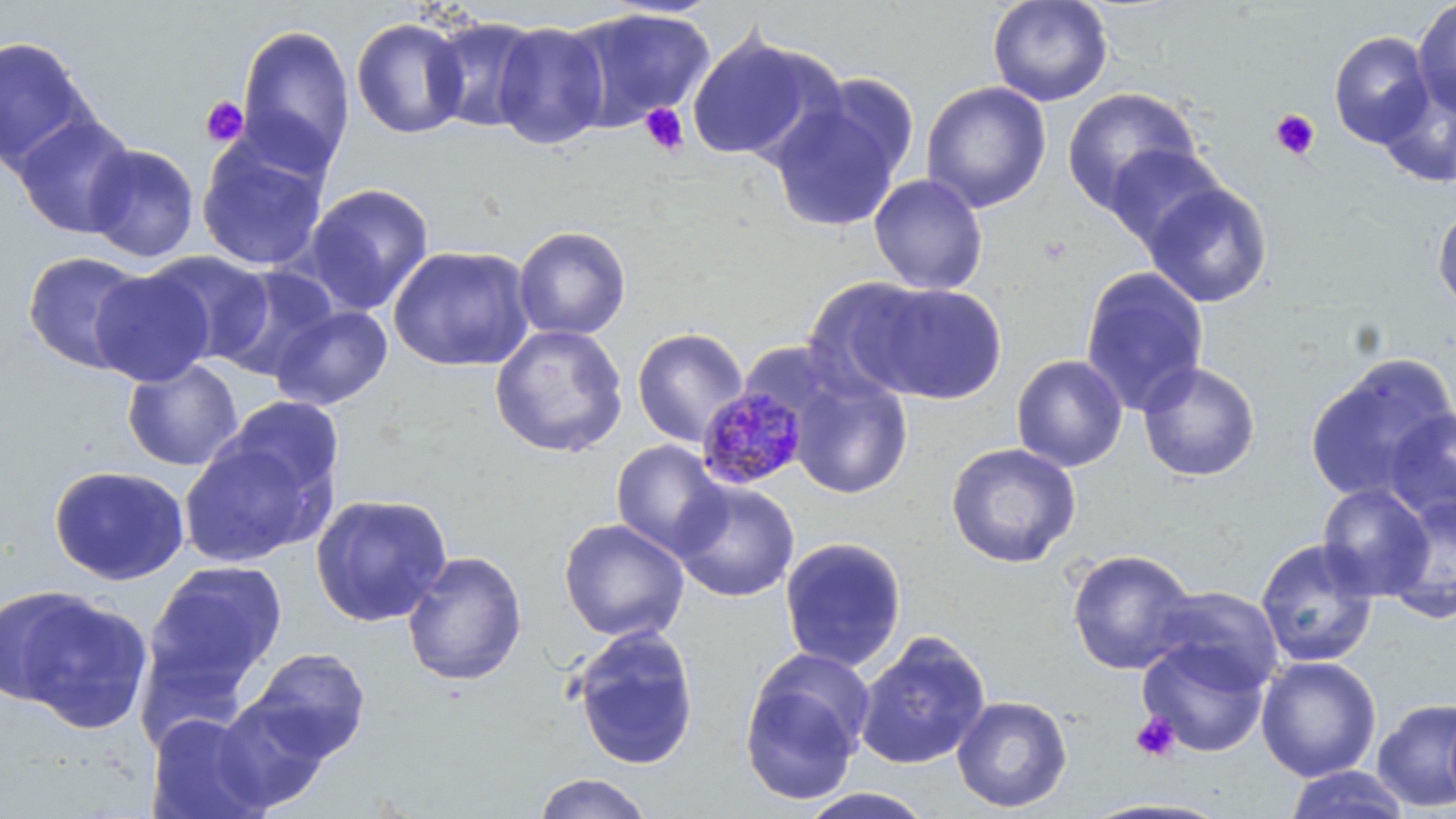

Approximate bounding boxes as named x1/y1/x2/y2 corners in pixels. Plasmodium malariae-infected red blood cell locations: (x1=696, y1=384, x2=811, y2=490). Uninfected red blood cell locations: (x1=987, y1=0, x2=1113, y2=107), (x1=1412, y1=0, x2=1456, y2=120), (x1=562, y1=6, x2=715, y2=132), (x1=427, y1=16, x2=544, y2=134), (x1=351, y1=17, x2=469, y2=140), (x1=493, y1=20, x2=610, y2=150), (x1=236, y1=24, x2=356, y2=172), (x1=686, y1=29, x2=836, y2=165), (x1=1329, y1=31, x2=1434, y2=148), (x1=0, y1=36, x2=97, y2=172), (x1=808, y1=71, x2=922, y2=187), (x1=1376, y1=78, x2=1456, y2=187), (x1=920, y1=80, x2=1052, y2=213), (x1=1061, y1=86, x2=1202, y2=214), (x1=767, y1=91, x2=908, y2=235), (x1=11, y1=112, x2=137, y2=238), (x1=196, y1=134, x2=329, y2=272), (x1=82, y1=143, x2=200, y2=263), (x1=1104, y1=144, x2=1228, y2=251), (x1=868, y1=174, x2=989, y2=295), (x1=1142, y1=181, x2=1273, y2=308), (x1=301, y1=183, x2=435, y2=316), (x1=1432, y1=203, x2=1456, y2=313), (x1=513, y1=225, x2=631, y2=341), (x1=388, y1=244, x2=535, y2=372), (x1=22, y1=250, x2=149, y2=374), (x1=144, y1=250, x2=275, y2=364), (x1=213, y1=264, x2=340, y2=382), (x1=1080, y1=266, x2=1210, y2=417), (x1=90, y1=269, x2=213, y2=387), (x1=802, y1=275, x2=934, y2=400), (x1=863, y1=282, x2=1007, y2=404), (x1=270, y1=305, x2=393, y2=410), (x1=489, y1=323, x2=628, y2=458), (x1=632, y1=327, x2=749, y2=447), (x1=1303, y1=353, x2=1456, y2=503), (x1=1011, y1=354, x2=1128, y2=472), (x1=122, y1=359, x2=243, y2=471), (x1=1137, y1=361, x2=1261, y2=482), (x1=787, y1=371, x2=913, y2=500), (x1=219, y1=396, x2=347, y2=508), (x1=1384, y1=405, x2=1455, y2=529), (x1=179, y1=437, x2=323, y2=566), (x1=611, y1=440, x2=728, y2=558), (x1=945, y1=442, x2=1082, y2=568), (x1=49, y1=464, x2=190, y2=585), (x1=670, y1=479, x2=800, y2=602), (x1=1316, y1=483, x2=1436, y2=601), (x1=310, y1=493, x2=453, y2=627), (x1=1380, y1=494, x2=1456, y2=625), (x1=558, y1=518, x2=690, y2=642), (x1=779, y1=536, x2=907, y2=672), (x1=1255, y1=538, x2=1380, y2=669), (x1=1066, y1=548, x2=1198, y2=675), (x1=401, y1=550, x2=528, y2=688), (x1=143, y1=560, x2=288, y2=702), (x1=1, y1=586, x2=152, y2=733), (x1=1149, y1=586, x2=1284, y2=693), (x1=567, y1=624, x2=700, y2=771), (x1=854, y1=631, x2=991, y2=771), (x1=1136, y1=638, x2=1269, y2=758), (x1=247, y1=647, x2=371, y2=763), (x1=739, y1=651, x2=872, y2=806), (x1=1255, y1=656, x2=1382, y2=782), (x1=210, y1=693, x2=334, y2=813), (x1=951, y1=695, x2=1073, y2=813), (x1=1372, y1=697, x2=1456, y2=812), (x1=145, y1=711, x2=271, y2=819), (x1=1283, y1=765, x2=1412, y2=818), (x1=530, y1=772, x2=655, y2=819), (x1=795, y1=788, x2=937, y2=818). Platelet locations: (x1=200, y1=96, x2=247, y2=147), (x1=639, y1=103, x2=690, y2=156), (x1=1270, y1=109, x2=1320, y2=160), (x1=1130, y1=712, x2=1181, y2=763). Slide-level diagnosis: Plasmodium malariae. One field of a larger specimen. 1000x magnification. Thin blood smear. Image is 1456×819 pixels. Optical microscopy. May-Grünwald-Giemsa stain.